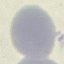

Summary:
  - Result: no malaria parasites seen
  - Capture: smartphone through the microscope eyepiece
  - Image type: cell patch, automatically extracted from a larger field of view and resized to 64 × 64 pixels
  - Preparation: thin smear
  - Stain: Giemsa